Classify this cell by malaria status.
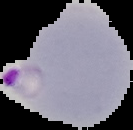
Parasitized.

Image is 133×130 pixels. From a thin blood film. Cell region segmented out of the field of view; the surrounding area is masked to black.